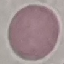

malaria status = uninfected
stain = Giemsa
capture = smartphone camera at the microscope eyepiece
preparation = thin blood film
image type = cell patch, automatically extracted from a larger field of view and resized to 64 × 64 pixels